Point out each leukocyte.
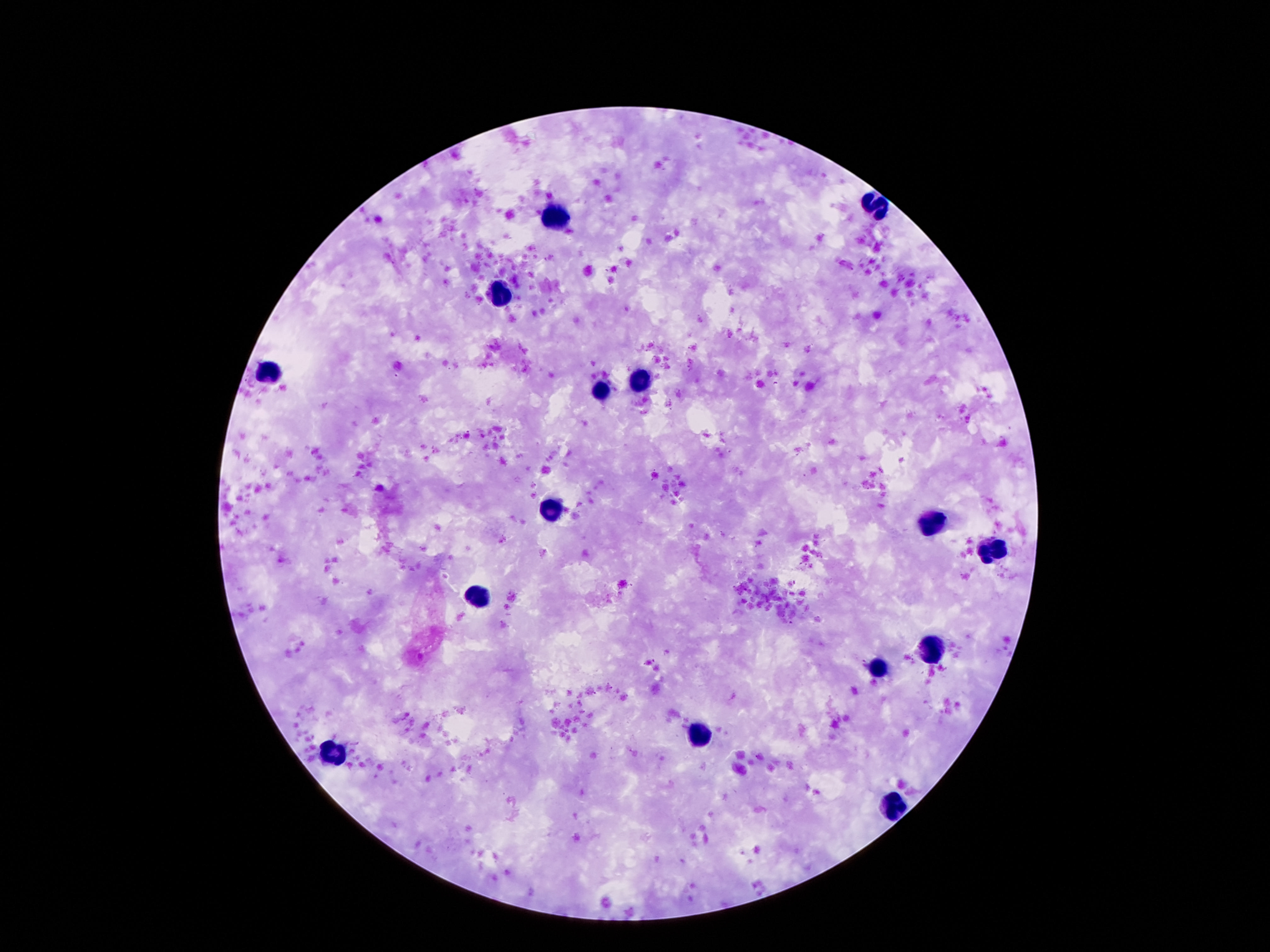
Approximate object centers, in pixels from the top-left corner.
Leukocytes: (x=875, y=206), (x=556, y=219), (x=505, y=292), (x=268, y=371), (x=635, y=380), (x=602, y=389), (x=551, y=512), (x=925, y=524), (x=995, y=553), (x=477, y=595), (x=932, y=646), (x=875, y=668), (x=700, y=736), (x=330, y=755), (x=891, y=802).

Summary:
  - Preparation: thick blood smear
  - Image size: 1270×952 pixels
  - Capture: smartphone camera through the microscope eyepiece
  - Patient malaria status: negative
  - Magnification: 100x
  - Field of view: one from this slide
  - Stain: Giemsa